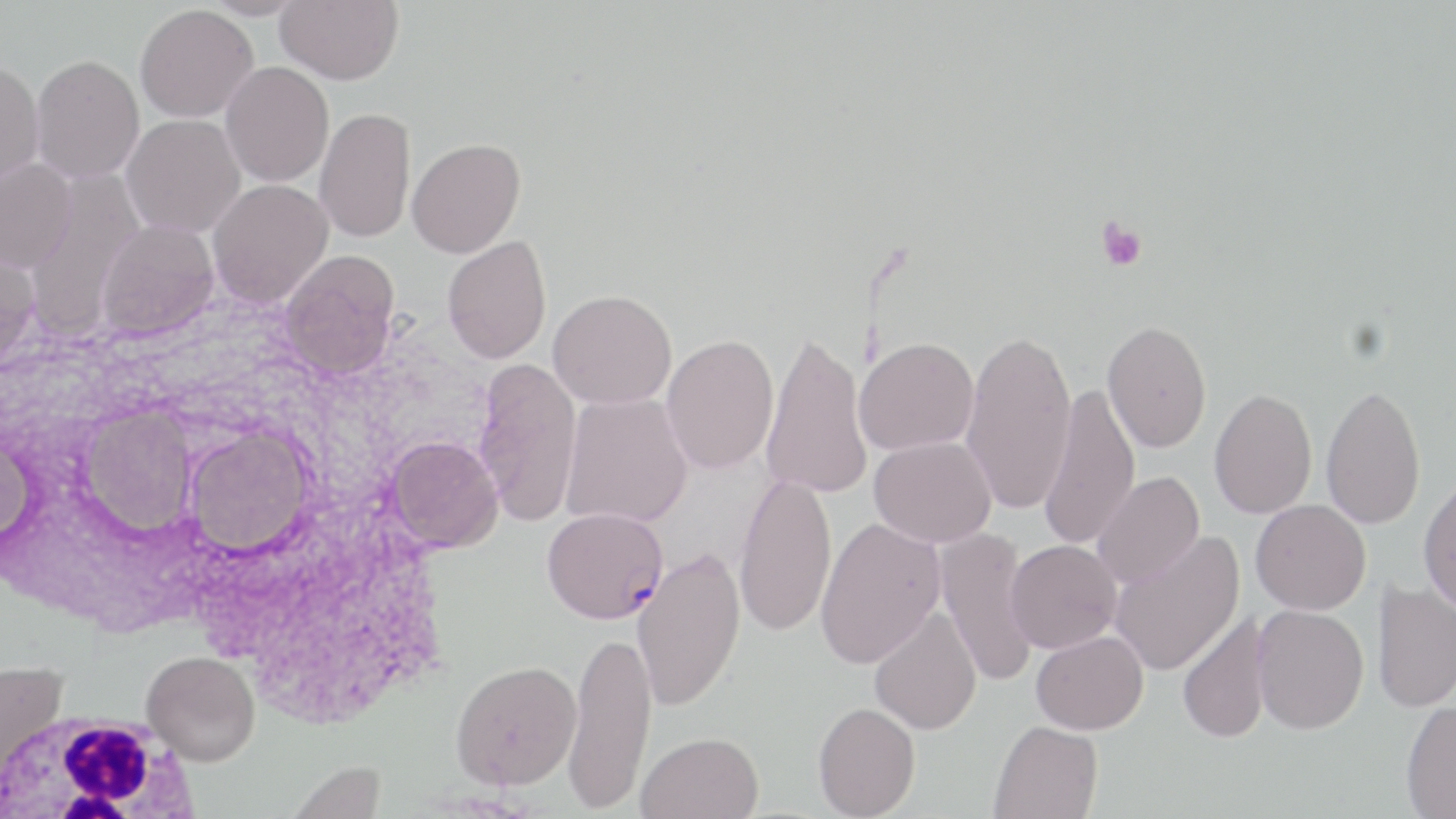

Approximate bounding boxes as (x1,y1)-(x2,y2) corner pairs in pixels. White blood cell locations: (0,708)-(202,816). Plasmodium falciparum-infected red blood cell locations: (542,508)-(670,624). Platelet locations: (1095,217)-(1148,272). Uninfected red blood cell locations: (199,0)-(312,20), (276,0)-(403,85), (134,4)-(258,123), (31,54)-(144,184), (0,60)-(45,191), (220,62)-(334,187), (314,107)-(416,244), (120,114)-(246,239), (407,137)-(526,258), (0,159)-(76,274), (23,174)-(147,336), (207,179)-(333,307), (96,220)-(219,340), (442,236)-(552,364), (0,249)-(40,374), (279,250)-(401,378), (548,289)-(677,409), (1103,320)-(1212,452), (960,325)-(1078,518), (759,329)-(873,500), (661,334)-(779,474), (854,338)-(979,455), (473,358)-(582,527), (1038,381)-(1140,553), (1320,383)-(1426,531), (1209,388)-(1318,519), (560,392)-(693,528), (76,405)-(197,537), (183,424)-(316,557), (0,430)-(37,552), (386,435)-(503,552), (869,435)-(997,548), (1092,471)-(1204,589), (734,472)-(837,638), (1417,475)-(1456,615), (1250,499)-(1371,615), (815,517)-(946,668), (934,528)-(1041,688), (1107,531)-(1245,677), (1006,539)-(1122,653), (632,547)-(746,712), (1373,581)-(1456,713), (1252,604)-(1369,734), (868,607)-(982,735), (1176,613)-(1271,745), (564,626)-(657,813), (1031,630)-(1148,734), (141,651)-(260,766), (450,659)-(581,790), (0,661)-(69,777), (812,701)-(921,818), (1400,701)-(1456,818), (988,719)-(1102,819), (636,731)-(764,819), (285,759)-(387,819). Slide-level diagnosis: Plasmodium falciparum. Captured at 1000x magnification. Thin blood film. May-Grünwald-Giemsa stain. Image is 1456×819 pixels. Single field of view. Light microscopy.